State which cell type is depicted.
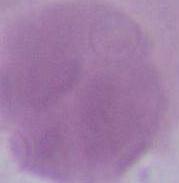
This is an erythrocyte.

magnification: 1000x
modality: micrograph